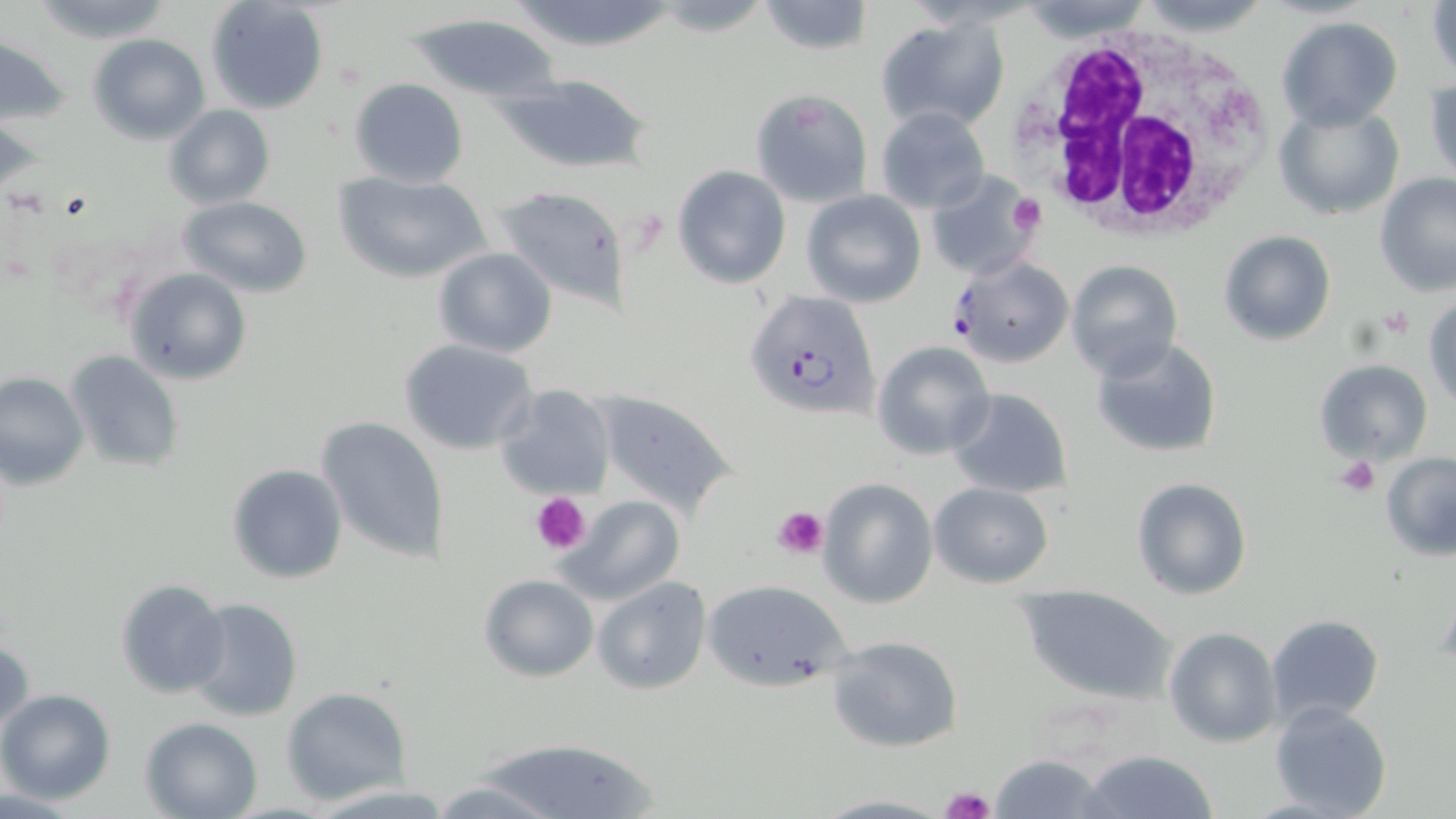

slide-level diagnosis = Plasmodium falciparum
modality = optical microscopy
white blood cell locations = approximate bounding boxes as [x1, y1, x2, y2] in pixels: [1015, 22, 1284, 242]
uninfected red blood cell locations = approximate bounding boxes as [x1, y1, x2, y2] in pixels: [28, 0, 175, 44], [205, 0, 330, 115], [756, 0, 872, 54], [1426, 2, 1456, 81], [403, 10, 563, 103], [874, 14, 1012, 135], [1275, 16, 1403, 130], [89, 33, 210, 144], [1, 37, 74, 125], [497, 74, 649, 173], [1424, 74, 1456, 188], [348, 78, 469, 187], [751, 89, 873, 207], [1271, 102, 1405, 221], [164, 104, 275, 209], [874, 107, 992, 214], [671, 164, 791, 289], [926, 170, 1040, 281], [332, 171, 493, 285], [1375, 174, 1456, 295], [494, 183, 631, 309], [802, 191, 926, 308], [179, 197, 312, 297], [1218, 230, 1336, 346], [432, 247, 558, 358], [1065, 260, 1183, 380], [125, 267, 252, 385], [1423, 292, 1455, 409], [1090, 337, 1223, 460], [398, 338, 538, 456], [872, 340, 994, 461], [64, 348, 185, 471], [1313, 358, 1433, 465], [0, 373, 88, 488], [495, 383, 616, 499], [946, 388, 1072, 497], [592, 391, 739, 515], [315, 415, 450, 564], [1380, 452, 1456, 559], [226, 463, 348, 584], [1132, 477, 1253, 601], [819, 478, 937, 608], [928, 482, 1054, 587], [558, 494, 685, 606], [479, 574, 599, 682], [592, 576, 711, 694], [115, 577, 230, 699], [700, 578, 854, 695], [1016, 582, 1179, 702], [182, 596, 304, 724], [1264, 613, 1385, 730], [1165, 626, 1282, 748], [1, 636, 33, 742], [829, 636, 964, 752], [281, 687, 410, 805], [0, 690, 116, 805], [1268, 701, 1392, 819], [140, 716, 264, 819], [471, 736, 665, 819], [1081, 749, 1219, 818], [989, 754, 1111, 818], [424, 779, 566, 816], [810, 792, 954, 817]
image size = 1456×819 pixels
stain = May-Grünwald-Giemsa
Plasmodium falciparum-infected red blood cell locations = approximate bounding boxes as [x1, y1, x2, y2] in pixels: [949, 257, 1072, 366], [743, 293, 885, 424]
platelet locations = approximate bounding boxes as [x1, y1, x2, y2] in pixels: [1008, 194, 1046, 237], [1378, 306, 1414, 341], [1336, 456, 1381, 497], [530, 491, 591, 556], [774, 504, 829, 557], [940, 786, 996, 819]
magnification = 1000x
field of view = single
preparation = thin blood film